Name the parasite shown.
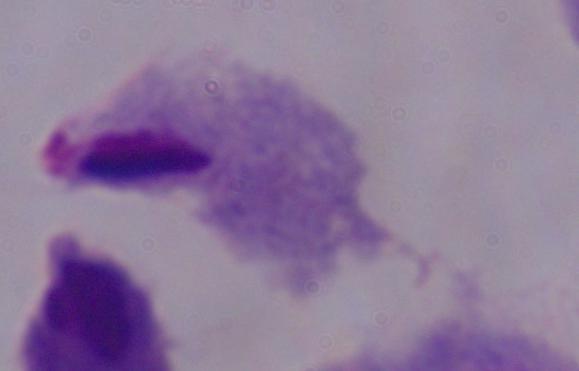
A trichomonad.

Captured at 1000x magnification. Photomicrograph.